Outline platelets.
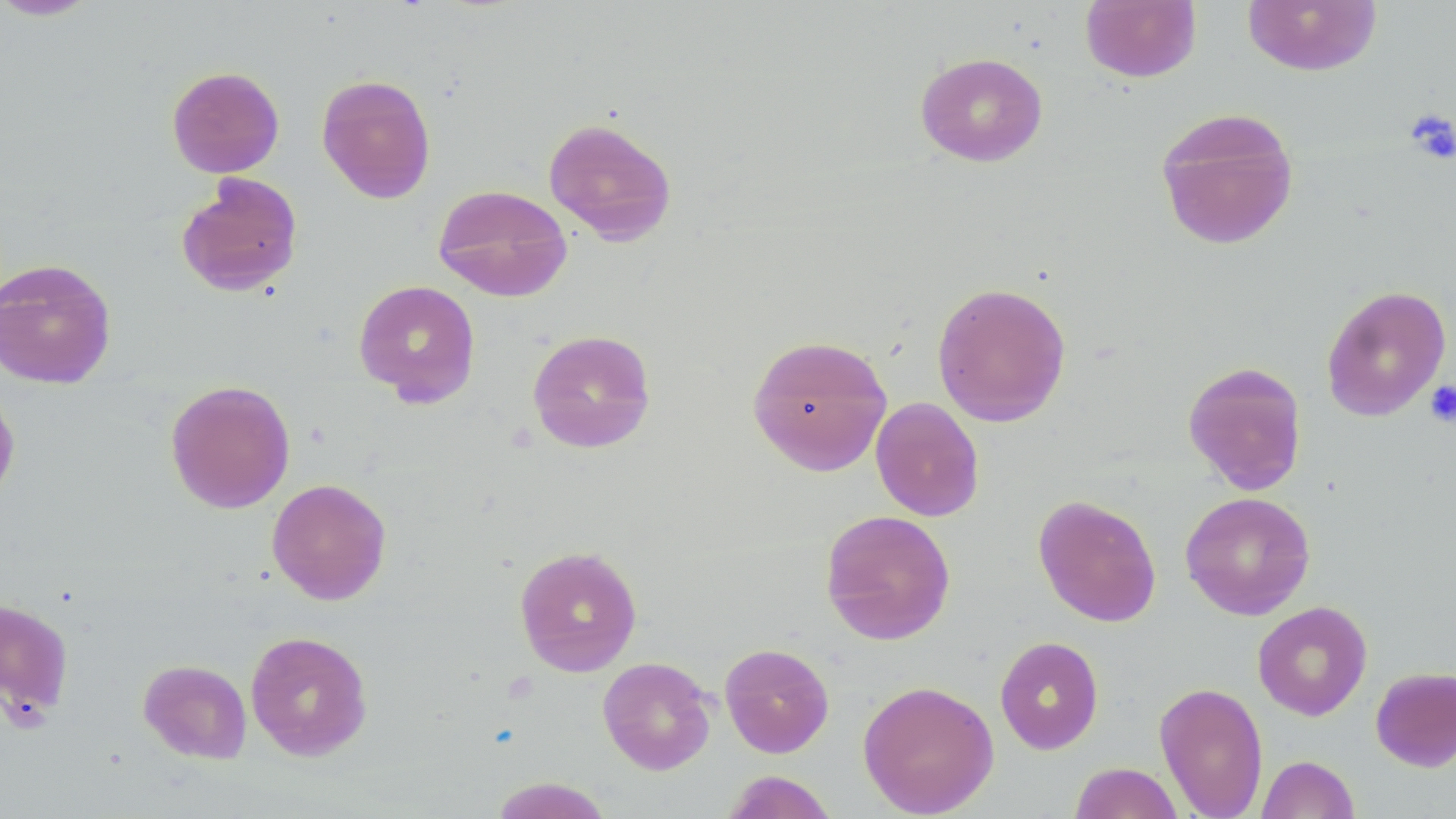

Approximate bounding boxes as (x1, y1, x2, y2) in pixels.
Platelets: (1404, 108, 1455, 165), (1424, 380, 1456, 427).

Summary:
  - Uninfected red blood cell locations: (0, 0, 102, 21), (1080, 0, 1201, 83), (1242, 0, 1382, 76), (915, 52, 1048, 167), (167, 65, 284, 178), (316, 73, 437, 204), (1154, 106, 1300, 250), (542, 116, 678, 245), (176, 173, 303, 297), (433, 184, 573, 302), (0, 258, 117, 389), (353, 279, 481, 407), (931, 281, 1072, 427), (1320, 284, 1451, 421), (527, 329, 656, 454), (746, 333, 892, 476), (1182, 361, 1308, 496), (165, 379, 295, 514), (0, 384, 21, 509), (870, 396, 985, 522), (267, 478, 392, 605), (1180, 491, 1315, 620), (1033, 494, 1162, 627), (819, 509, 957, 645), (513, 545, 643, 677), (0, 596, 75, 724), (1252, 600, 1373, 721), (245, 630, 373, 761), (994, 636, 1104, 755), (719, 642, 834, 758), (598, 656, 716, 775), (138, 659, 252, 764), (1371, 666, 1456, 772), (857, 679, 999, 817), (1154, 681, 1269, 819), (1256, 755, 1360, 819), (1069, 762, 1183, 819), (720, 771, 839, 818), (488, 777, 614, 818)
  - Slide-level diagnosis: no evidence of blood parasites
  - Preparation: thin blood smear
  - Stain: May-Grünwald-Giemsa
  - Field of view: single
  - Modality: light microscopy
  - Magnification: 1000x
  - Image size: 1456×819 pixels